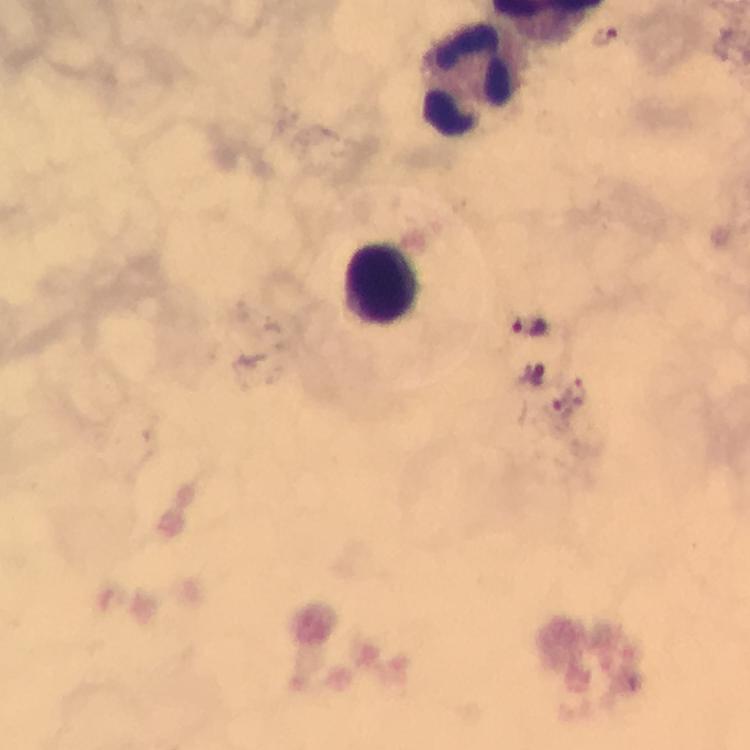
Approximate object centers, in pixels from the top-left corner. Leukocyte locations: (x=476, y=79), (x=385, y=281). Plasmodium parasite locations: (x=531, y=326), (x=562, y=400). From a diagnostic examination for malaria. Smartphone photograph taken through a microscope. Thick blood film. Image is 750×750 pixels. 100x magnification. A crop from one field of view. Immersion oil was used. Giemsa-stained preparation.